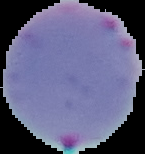
Result: Plasmodium parasites identified. Cell region segmented out of the field of view; the surrounding area is masked to black. Image is 145×154 pixels. From a thin blood smear.